Assess for malaria.
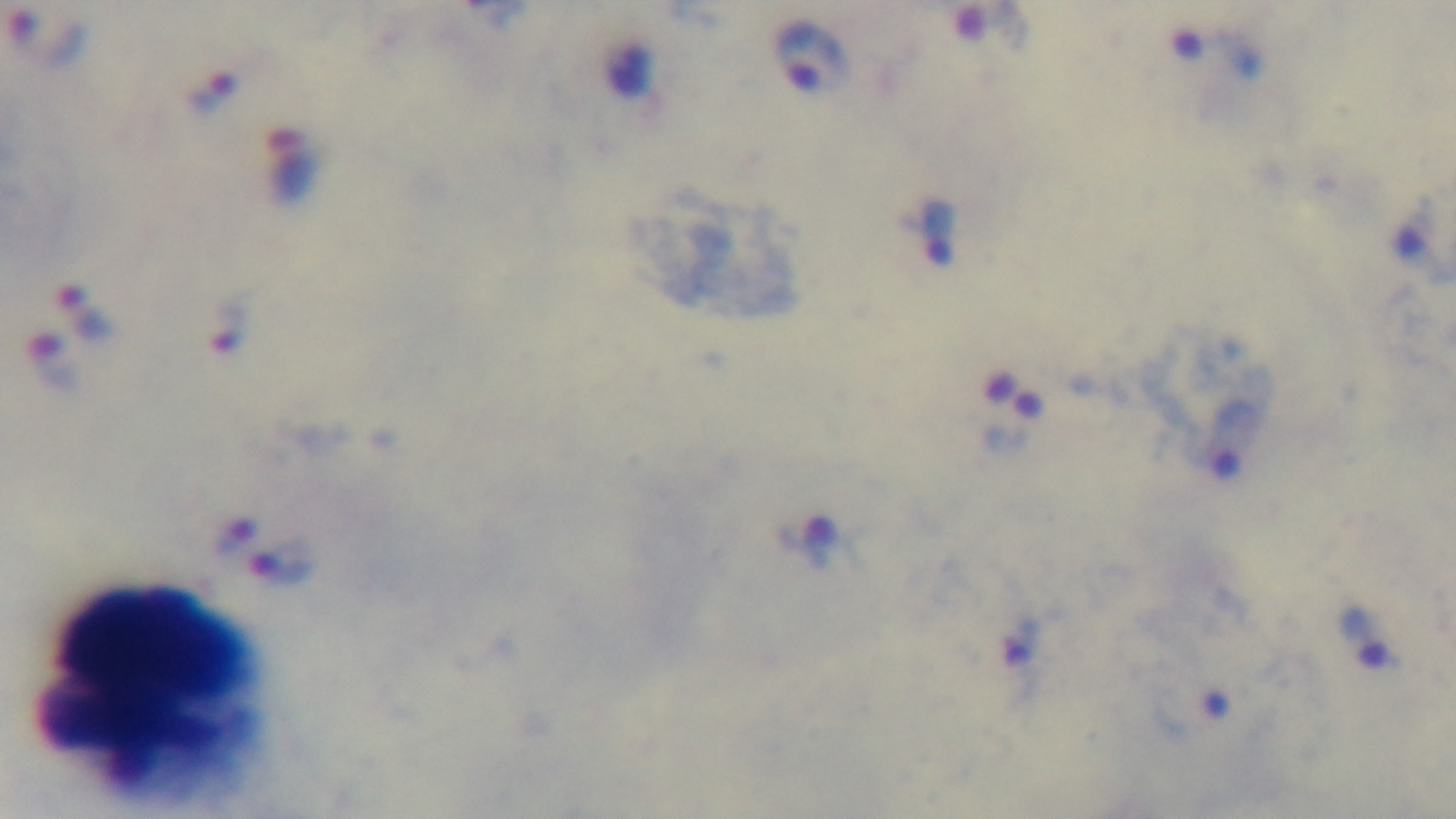
Infected.

preparation = thick
capture = mounted 4K digital camera
stain = Giemsa
modality = light microscopy
objective = 100x oil immersion
field of view = one from the slide